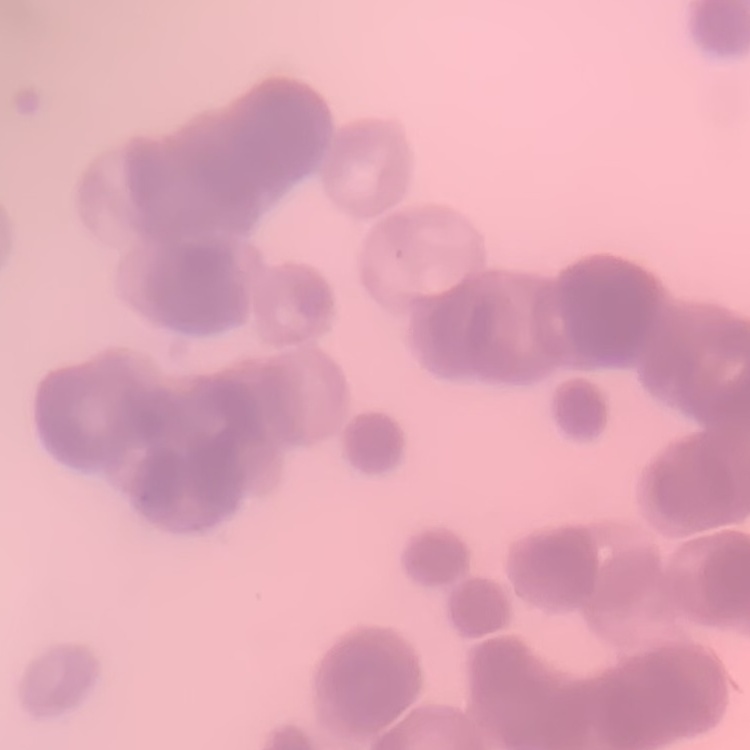

The red blood cells exhibit rouleaux formation. Square crop of a larger photomicrograph. Stained with either Field's or Giemsa. Thin blood smear.